Give the position of every malaria parasite.
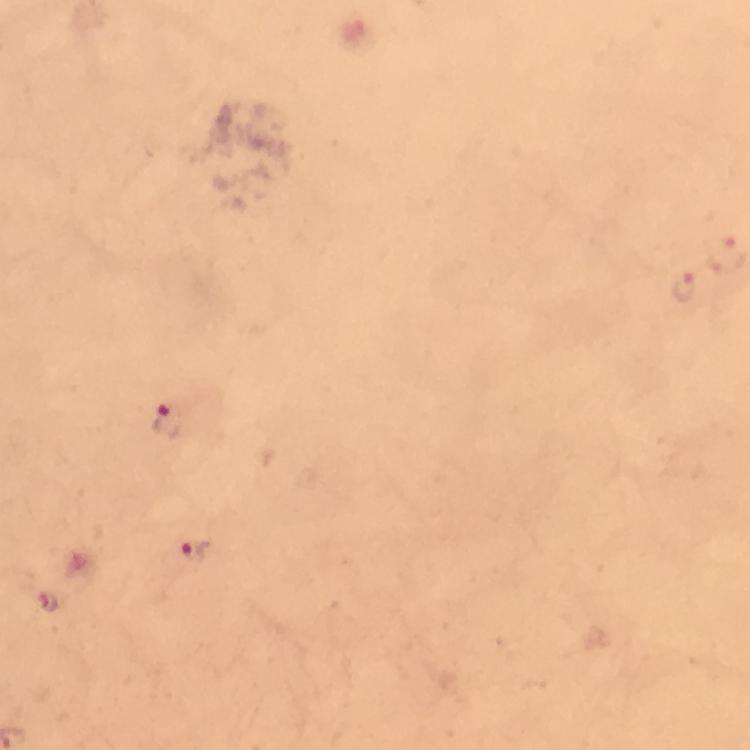

Approximate centers as [x, y] in pixels.
Malaria parasites: [684, 287], [170, 425], [195, 551], [48, 602].

cropped from = one field of view
preparation = thick smear
immersion oil = applied
magnification = 100x
context = from a malaria diagnostic workup
capture = smartphone photograph through a microscope
stain = Giemsa
image size = 750×750 pixels